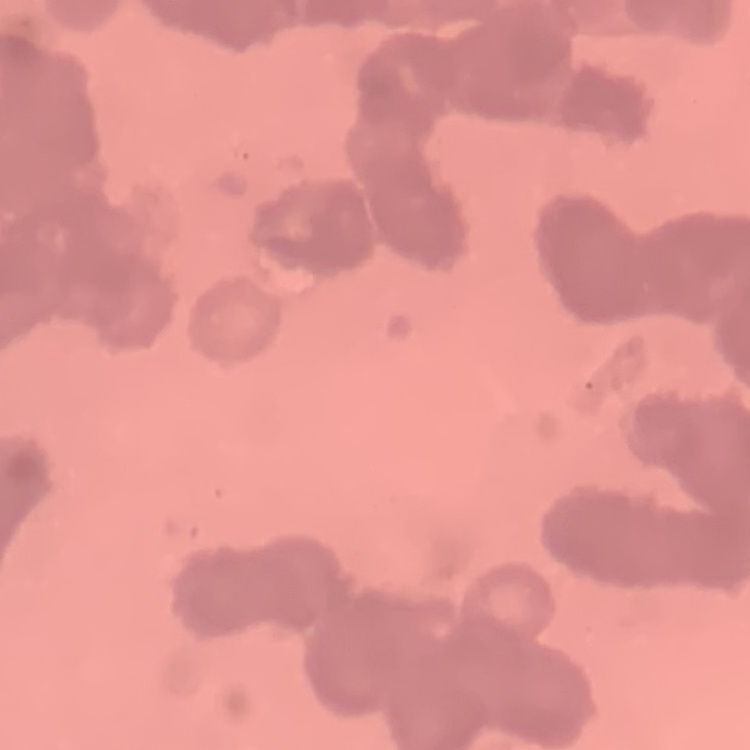

Summary:
  - Red blood cell morphology: rouleaux formation
  - Preparation: thin blood film
  - Image type: square crop of a larger photomicrograph
  - Stain: Field's or Giemsa